Assess the morphology of the erythrocytes.
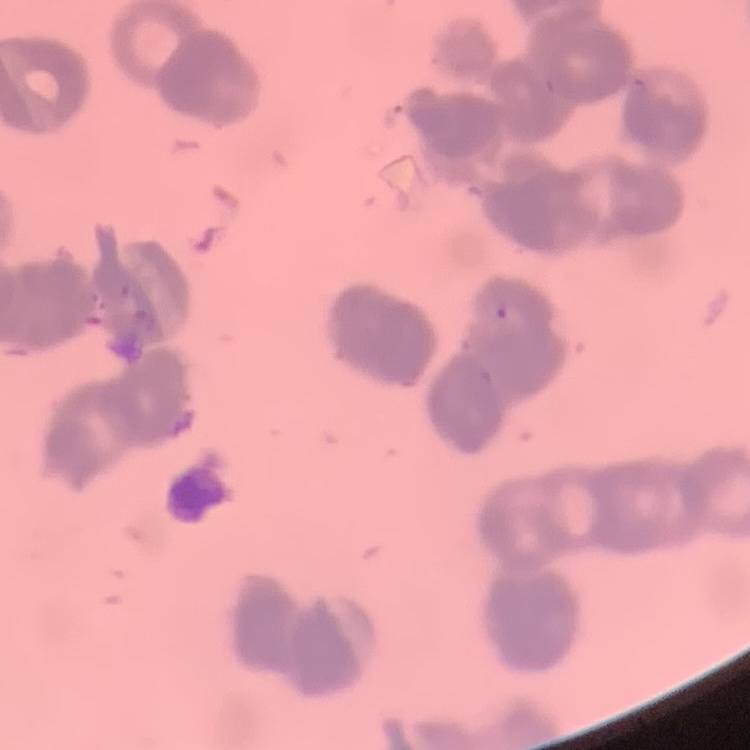
Rouleaux formation.

One tile cut from a larger photomicrograph. Stained with either Field's or Giemsa. Thin blood smear.